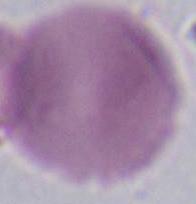

Captured at 1000x magnification. Micrograph. An erythrocyte is shown.